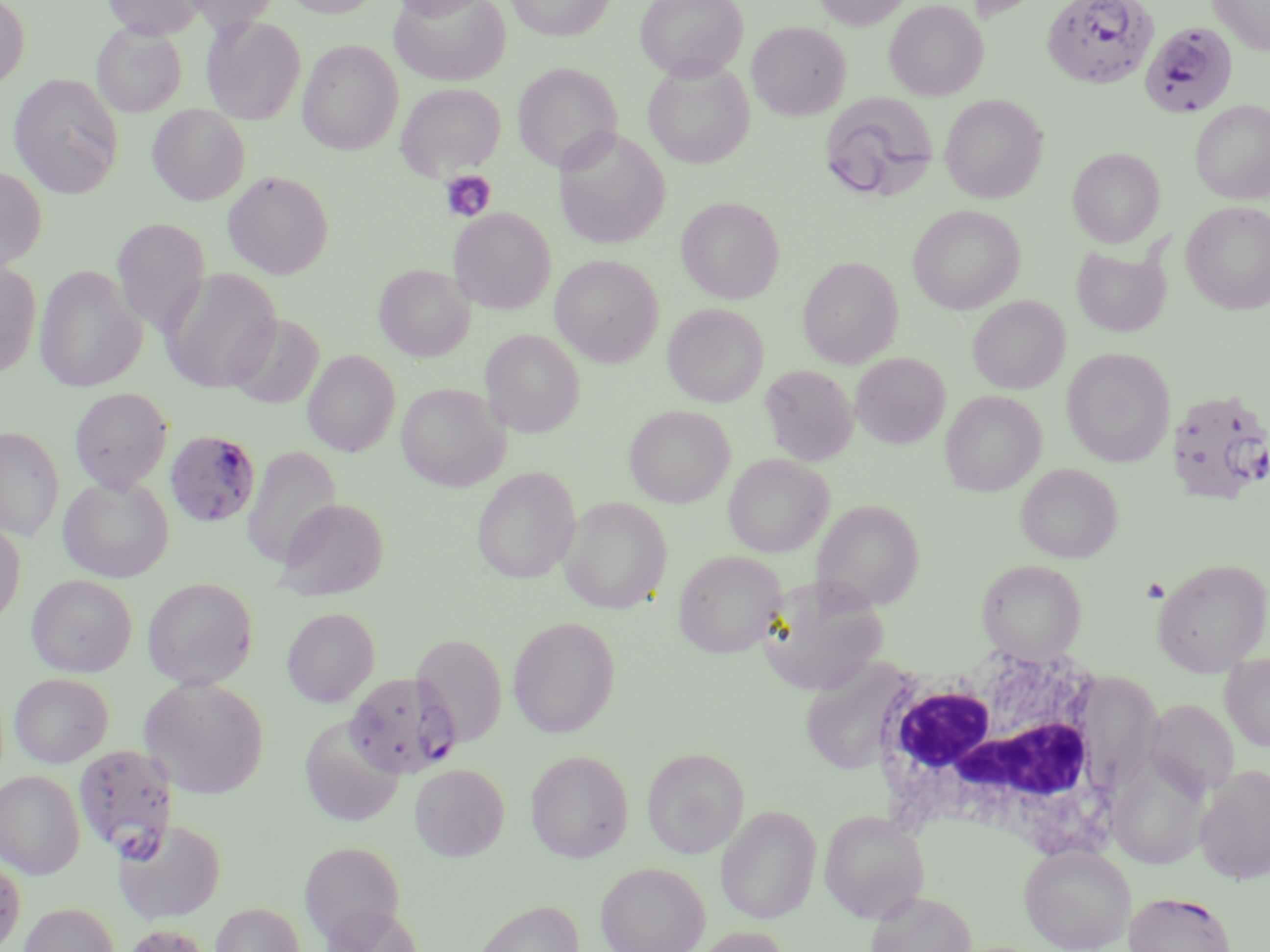
slide_level_diagnosis: Plasmodium falciparum
magnification: 1000x
field_of_view: single
image_size: 1270×952 pixels
preparation: thin blood film
white_blood_cell_locations: 'approximate bounding boxes as (x1, y1, x2, y2) in pixels: (868, 641, 1123, 857)'
modality: light microscopy
uninfected_red_blood_cell_locations: 'approximate bounding boxes as (x1, y1, x2, y2) in pixels: (0, 0, 31, 90), (102, 0, 205, 38), (184, 0, 281, 32), (284, 0, 381, 17), (389, 0, 494, 20), (391, 0, 510, 85), (506, 0, 615, 40), (635, 0, 748, 81), (813, 0, 913, 30), (884, 0, 988, 100), (961, 0, 1054, 24), (1208, 0, 1270, 56), (202, 16, 305, 124), (747, 22, 851, 120), (92, 23, 187, 117), (298, 40, 403, 155), (643, 59, 755, 168), (513, 62, 622, 173), (9, 73, 125, 198), (396, 83, 506, 180), (818, 92, 941, 205), (940, 94, 1047, 203), (1190, 100, 1270, 204), (148, 104, 250, 205), (554, 128, 671, 249), (1068, 147, 1165, 248), (0, 166, 47, 272), (223, 171, 334, 279), (676, 196, 785, 304), (1181, 201, 1270, 314), (907, 205, 1025, 314), (449, 207, 555, 314), (111, 218, 210, 336), (1071, 242, 1171, 338), (550, 254, 664, 367), (798, 256, 903, 369), (0, 258, 42, 379), (34, 264, 146, 393), (374, 264, 476, 361), (159, 267, 282, 393), (968, 295, 1070, 394), (663, 303, 768, 407), (228, 313, 324, 409), (480, 329, 585, 437), (1062, 348, 1175, 467), (303, 350, 400, 456), (851, 352, 950, 448), (760, 364, 859, 465), (396, 382, 510, 491), (69, 388, 173, 493), (941, 390, 1046, 496), (624, 404, 735, 507), (0, 426, 65, 541), (242, 446, 341, 568), (723, 453, 834, 557), (1016, 463, 1122, 562), (472, 466, 580, 584), (58, 474, 174, 582), (558, 497, 672, 613), (274, 498, 388, 600), (812, 499, 925, 611), (0, 518, 26, 626), (674, 550, 786, 658), (1151, 557, 1270, 675), (977, 559, 1086, 661), (26, 574, 137, 677), (755, 576, 887, 695), (142, 577, 258, 690), (282, 608, 379, 706), (508, 616, 620, 738), (411, 633, 507, 747), (1220, 652, 1270, 752), (798, 656, 912, 775), (9, 673, 113, 768), (140, 677, 270, 799), (300, 718, 404, 827), (1105, 746, 1212, 870), (642, 747, 749, 858), (526, 750, 633, 863), (409, 764, 509, 861), (1194, 765, 1270, 884), (0, 770, 85, 878), (716, 805, 822, 924), (819, 810, 930, 923), (113, 818, 227, 925), (300, 841, 405, 945), (1019, 843, 1136, 952), (0, 854, 25, 952), (596, 861, 710, 952), (866, 890, 977, 952), (473, 898, 584, 952), (19, 902, 119, 952), (210, 902, 306, 952), (319, 904, 426, 952), (123, 924, 212, 952), (691, 926, 793, 952)'
stain: May-Grünwald-Giemsa
plasmodium_falciparum_infected_red_blood_cell_locations: 'approximate bounding boxes as (x1, y1, x2, y2) in pixels: (1042, 0, 1159, 89), (1139, 24, 1237, 123), (1166, 388, 1269, 506), (165, 428, 262, 529), (345, 671, 462, 779), (73, 743, 180, 859), (1125, 891, 1235, 952)'
platelet_locations: 'approximate bounding boxes as (x1, y1, x2, y2) in pixels: (439, 170, 496, 223)'